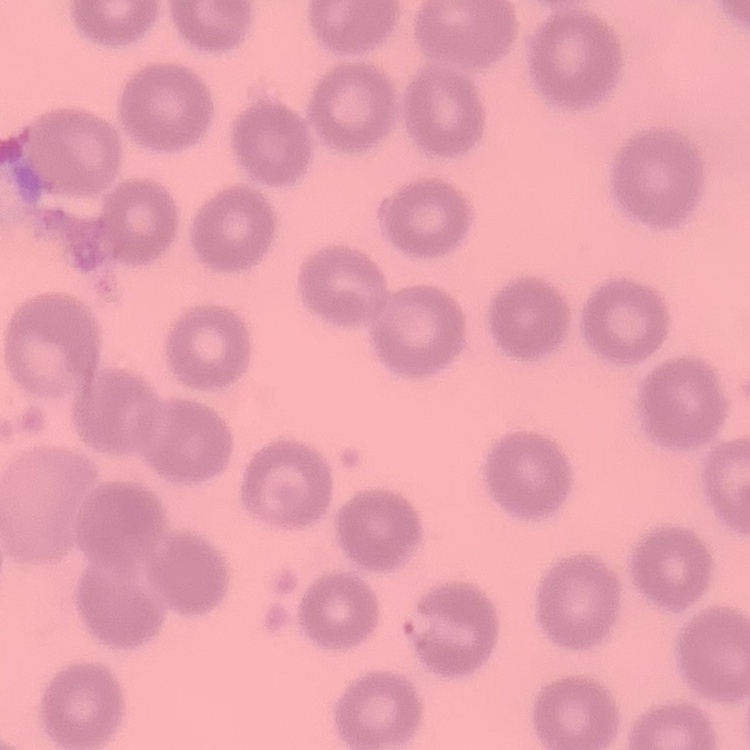

Summary:
  - Erythrocyte morphology: no rouleaux formation
  - Preparation: thin blood smear
  - Stain: Field's or Giemsa
  - Image type: one tile cut from a larger photomicrograph